Give the position of every Plasmodium parasite visible.
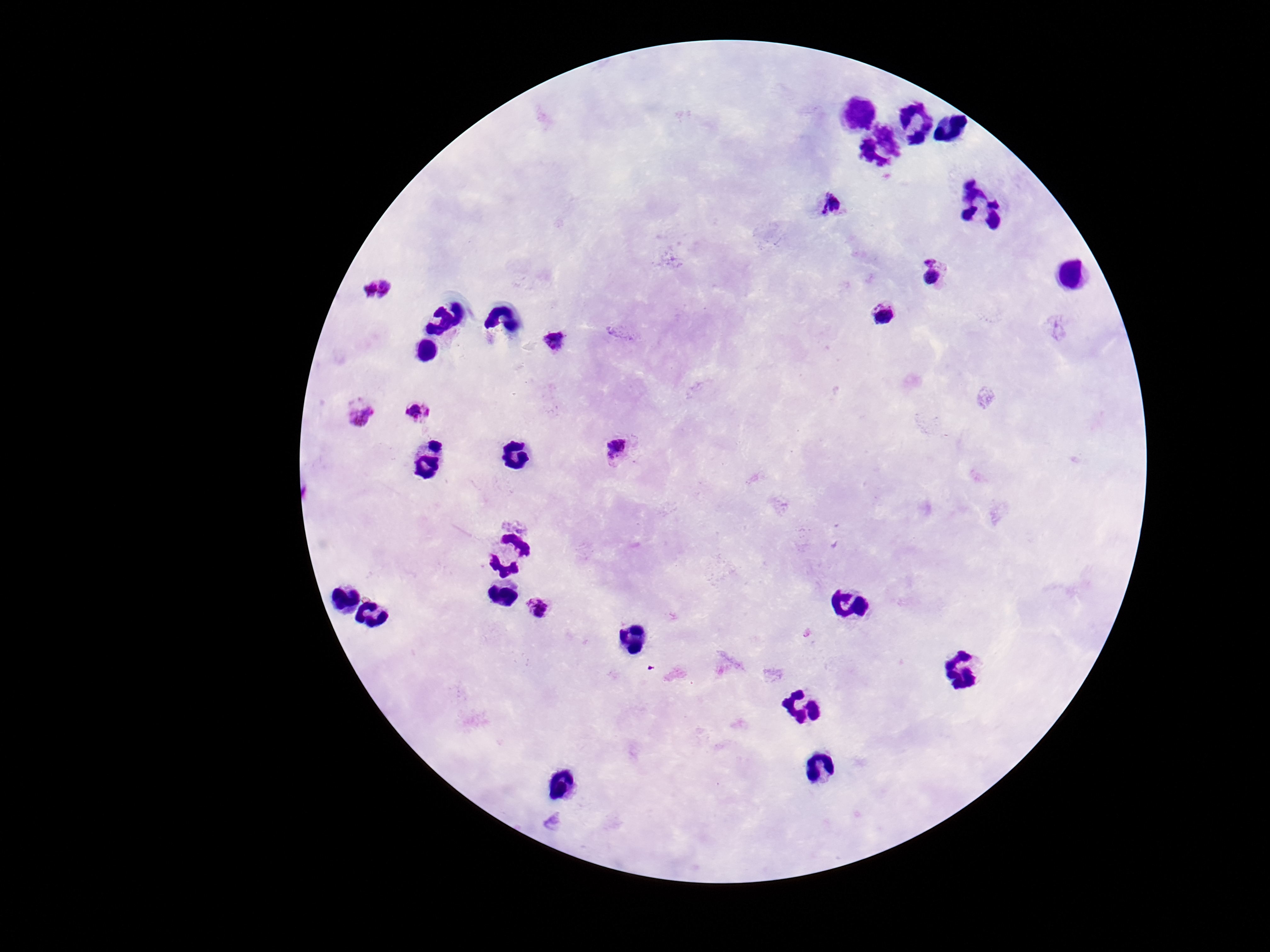

Approximate object centers, in pixels from the top-left corner.
Plasmodium parasites: (x=829, y=204), (x=932, y=272), (x=378, y=288), (x=885, y=314), (x=556, y=339), (x=357, y=411), (x=420, y=411), (x=618, y=450), (x=540, y=611).

Summary:
  - Patient malaria status: infected
  - Field of view: single
  - Preparation: thick blood film
  - Image size: 1270×952 pixels
  - Stain: Giemsa
  - Capture: smartphone camera through the microscope eyepiece
  - Magnification: 100x